Locate and identify every blood parasite.
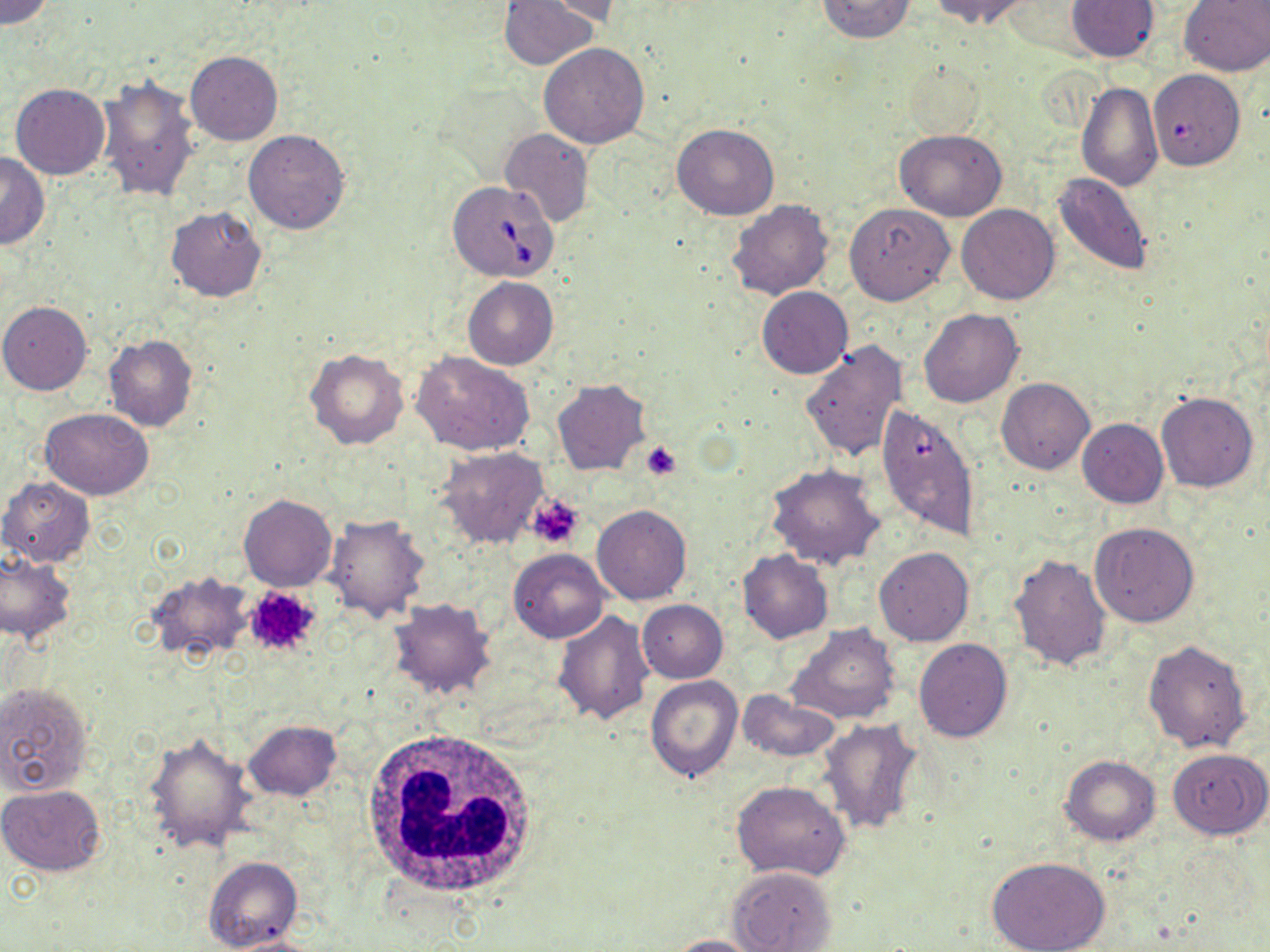
Approximate bounding boxes as (x1, y1, x2, y2) in pixels.
Babesia divergens-infected red blood cells: (447, 180, 560, 283), (878, 402, 981, 543).
No Plasmodium falciparum, Plasmodium ovale, Plasmodium malariae, Plasmodium vivax, or Trypanosoma brucei observed.

Uninfected red blood cell locations: (1, 0, 55, 28), (499, 0, 601, 71), (815, 0, 917, 42), (932, 0, 1034, 26), (1066, 0, 1160, 61), (1179, 0, 1270, 75), (537, 1, 631, 26), (538, 43, 649, 148), (185, 51, 283, 146), (903, 62, 982, 138), (1149, 69, 1248, 174), (96, 74, 199, 203), (1076, 81, 1162, 193), (10, 82, 110, 179), (671, 123, 779, 219), (894, 128, 1007, 221), (499, 129, 593, 229), (243, 130, 350, 234), (0, 152, 48, 248), (1052, 173, 1155, 276), (726, 199, 836, 302), (845, 203, 955, 304), (956, 203, 1060, 305), (166, 206, 267, 302), (463, 276, 558, 369), (757, 286, 853, 379), (0, 302, 92, 395), (919, 309, 1024, 408), (104, 335, 197, 433), (800, 339, 909, 463), (305, 349, 409, 450), (412, 350, 536, 457), (996, 377, 1094, 474), (553, 379, 650, 476), (1156, 391, 1258, 493), (40, 408, 155, 500), (1076, 419, 1168, 508), (436, 448, 549, 549), (767, 464, 885, 570), (0, 476, 94, 566), (239, 493, 338, 591), (591, 504, 691, 604), (322, 513, 429, 622), (1090, 521, 1200, 628), (874, 548, 974, 647), (509, 549, 610, 643), (739, 550, 832, 644), (0, 552, 76, 644), (1008, 553, 1111, 672), (147, 570, 252, 661), (387, 599, 497, 699), (637, 599, 728, 683), (553, 610, 654, 725), (787, 623, 900, 725), (1142, 638, 1253, 753), (913, 639, 1013, 742), (645, 675, 742, 783), (0, 681, 93, 796), (736, 691, 842, 764), (244, 719, 341, 800), (818, 719, 924, 835), (144, 732, 255, 853), (1167, 748, 1270, 839), (1059, 754, 1161, 846), (731, 779, 851, 881), (0, 784, 107, 876), (984, 855, 1111, 952), (204, 857, 302, 951), (729, 866, 838, 952), (218, 933, 321, 952), (667, 935, 767, 952). Platelet locations: (641, 440, 681, 479), (527, 494, 583, 549), (241, 586, 324, 660). White blood cell locations: (362, 728, 538, 900). Slide-level diagnosis: Babesia divergens. Image is 1270×952 pixels. May-Grünwald-Giemsa stain. Thin blood film. Captured at 1000x magnification. Optical microscopy. One field of a larger specimen.